Identify the blood parasite species.
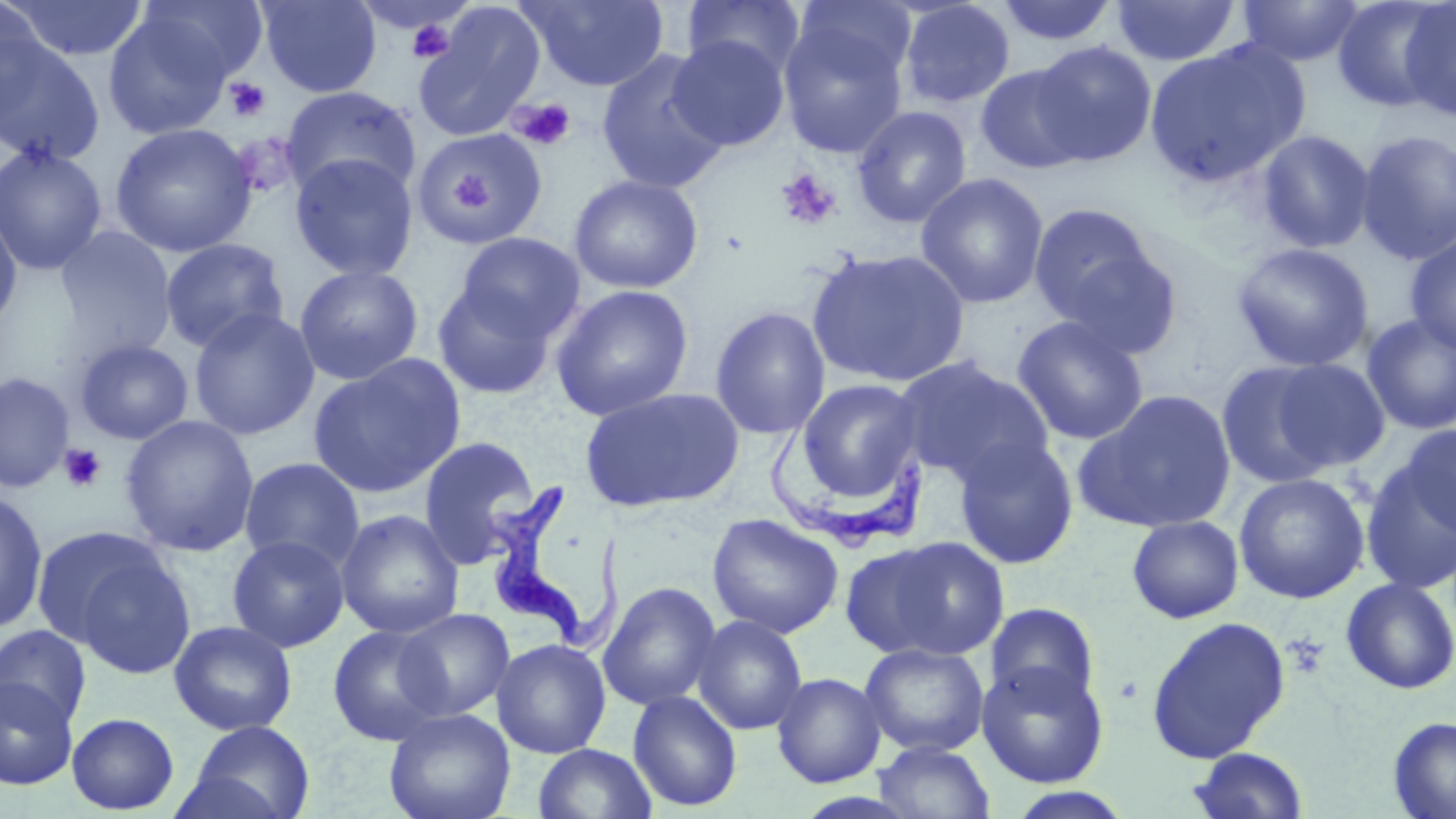
Trypanosoma brucei.

image size = 1456×819 pixels
stain = May-Grünwald-Giemsa
preparation = thin blood film
platelet locations = approximate bounding boxes as [x1, y1, x2, y2] in pixels: [402, 12, 459, 62], [223, 77, 272, 123], [507, 96, 577, 151], [774, 168, 842, 231], [60, 444, 107, 492], [1285, 633, 1328, 677]
Trypanosoma brucei locations = approximate bounding boxes as [x1, y1, x2, y2] in pixels: [769, 417, 928, 553], [483, 485, 621, 650]
modality = light microscopy
uninfected red blood cell locations = approximate bounding boxes as [x1, y1, x2, y2] in pixels: [3, 0, 150, 62], [256, 0, 382, 98], [520, 0, 669, 92], [681, 0, 807, 80], [995, 0, 1119, 46], [1332, 0, 1451, 114], [0, 1, 45, 120], [135, 1, 268, 86], [898, 1, 1016, 109], [1111, 1, 1241, 67], [1235, 1, 1367, 67], [792, 2, 918, 93], [1397, 2, 1456, 122], [413, 3, 546, 141], [102, 7, 240, 141], [778, 13, 909, 160], [0, 29, 106, 166], [667, 35, 790, 151], [1146, 39, 1310, 185], [1030, 41, 1158, 166], [595, 50, 731, 195], [974, 64, 1091, 174], [280, 87, 421, 199], [852, 105, 972, 228], [110, 123, 257, 257], [414, 128, 549, 247], [1356, 128, 1456, 266], [1256, 130, 1376, 253], [0, 144, 108, 275], [289, 153, 418, 281], [453, 166, 493, 208], [915, 172, 1049, 309], [568, 174, 704, 294], [1027, 202, 1164, 330], [0, 206, 22, 333], [54, 226, 177, 359], [455, 232, 585, 343], [1404, 233, 1456, 355], [160, 238, 288, 353], [1232, 241, 1374, 372], [1052, 242, 1185, 360], [807, 248, 970, 388], [294, 264, 423, 385], [432, 280, 558, 399], [551, 284, 693, 420], [709, 305, 831, 440], [189, 307, 320, 440], [1361, 314, 1456, 435], [1011, 315, 1149, 445], [74, 339, 193, 445], [308, 354, 465, 498], [894, 356, 1055, 486], [1215, 359, 1344, 489], [1268, 359, 1392, 472], [0, 372, 74, 493], [794, 377, 925, 510], [579, 386, 745, 513], [1074, 389, 1237, 534], [120, 414, 259, 557], [1396, 425, 1456, 541], [417, 435, 542, 568], [952, 436, 1079, 569], [1360, 455, 1456, 595], [239, 457, 365, 573], [1233, 472, 1370, 604], [0, 489, 48, 634], [335, 509, 464, 638], [706, 513, 844, 638], [1127, 515, 1244, 623], [31, 528, 167, 647], [227, 534, 350, 652], [845, 534, 1010, 664], [72, 554, 198, 682], [1340, 577, 1456, 695], [598, 581, 722, 711], [984, 602, 1102, 708], [396, 608, 515, 720], [692, 615, 808, 735], [1145, 615, 1291, 764], [169, 620, 297, 736], [327, 624, 450, 747], [0, 625, 91, 729], [491, 638, 611, 758], [859, 642, 989, 757], [976, 661, 1109, 788], [771, 672, 886, 788], [0, 676, 78, 790], [627, 690, 743, 812], [383, 707, 516, 819], [67, 712, 180, 814], [1388, 716, 1456, 819], [183, 720, 316, 819], [872, 741, 996, 819], [532, 743, 658, 819], [1188, 747, 1309, 819], [1002, 786, 1136, 818]
magnification = 1000x
field of view = single